Assess the morphology of the red blood cells.
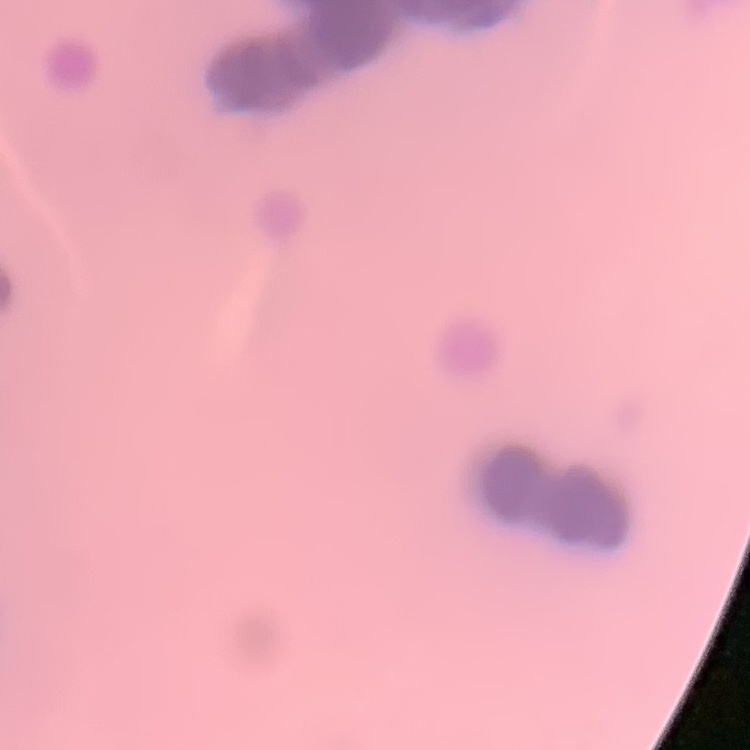

They show rouleaux formation.

stain = Field's or Giemsa
image type = square crop of a larger photomicrograph
preparation = thin blood smear